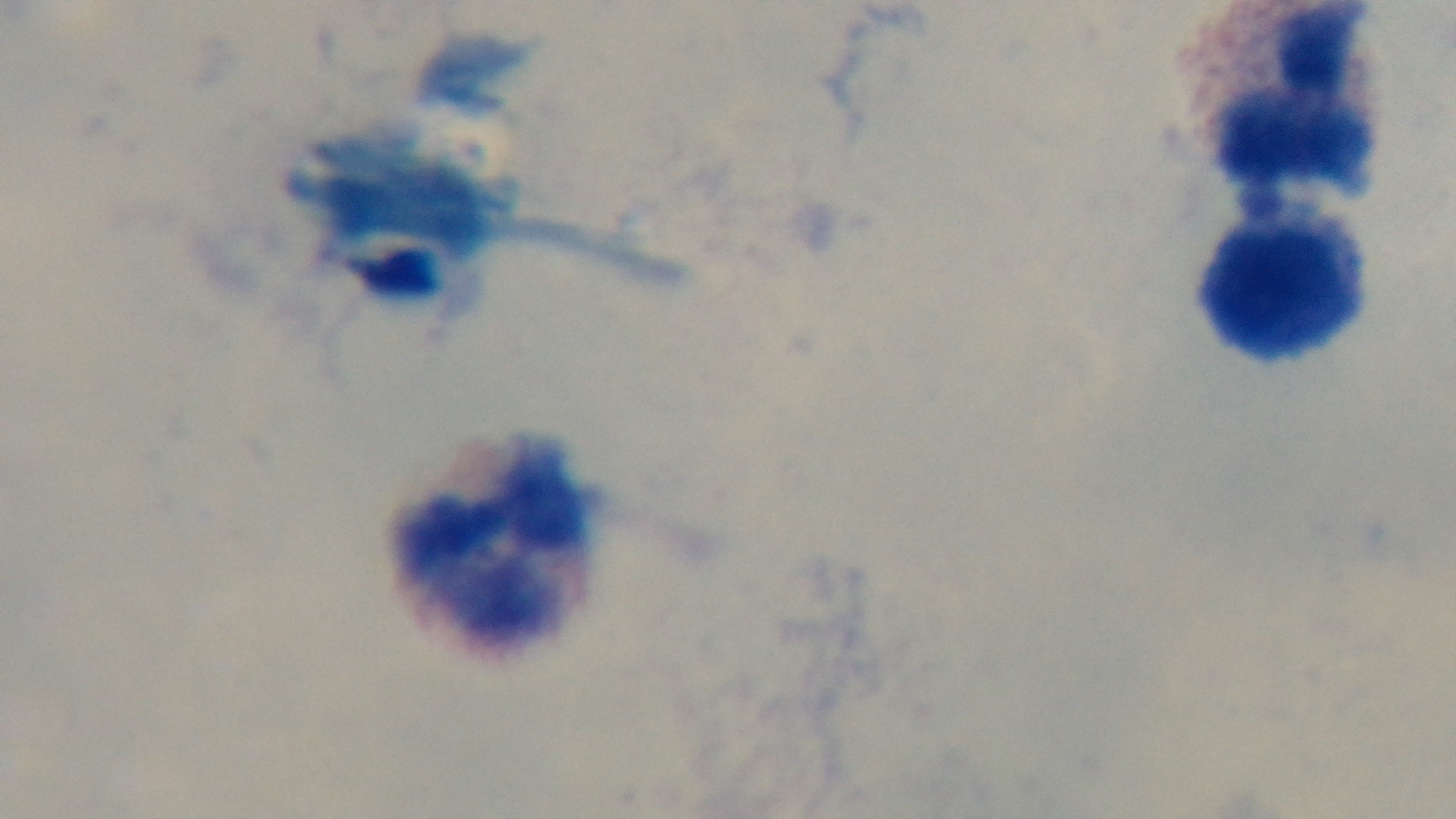

Summary:
  - Modality: light microscopy
  - Capture: mounted 4K digital camera
  - Field of view: one from the slide
  - Objective: 100x oil immersion
  - Stain: Giemsa
  - Preparation: thick blood film
  - Malaria status: uninfected